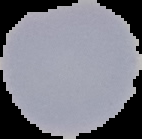

image_size: 142×139 pixels
result: no malaria parasites detected
image_type: segmented cell region on a black background
preparation: thin blood film